Give the position of every Plasmodium parasite.
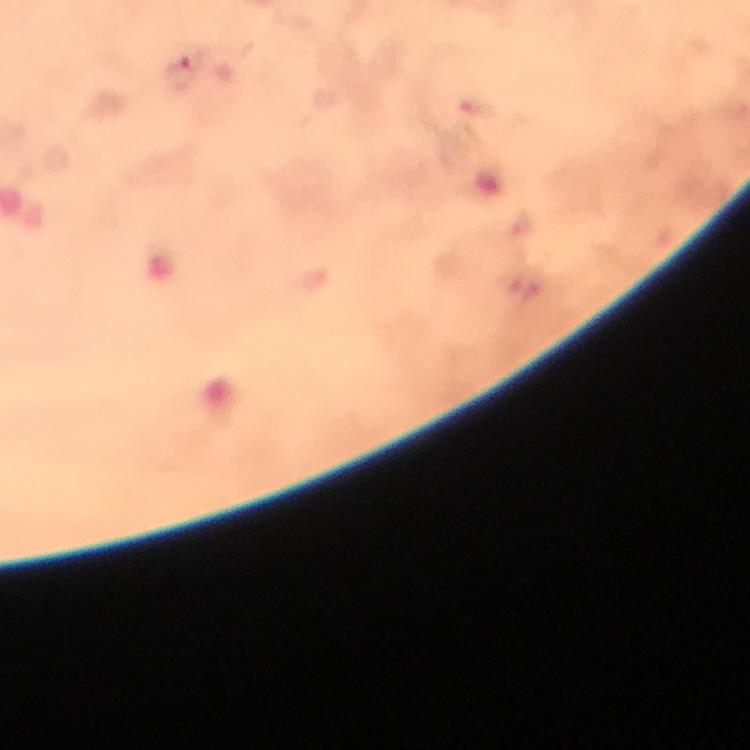
Approximate centers as (x, y) in pixels.
Plasmodium parasites: (179, 76).

capture = smartphone mounted on the microscope
image size = 750×750 pixels
magnification = 100x
context = from a malaria diagnostic workup
stain = Giemsa
cropped from = one field of view
immersion oil = used
preparation = thick blood smear